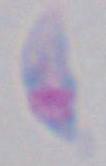

modality = photomicrograph
identification = Toxoplasma gondii
magnification = 1000x